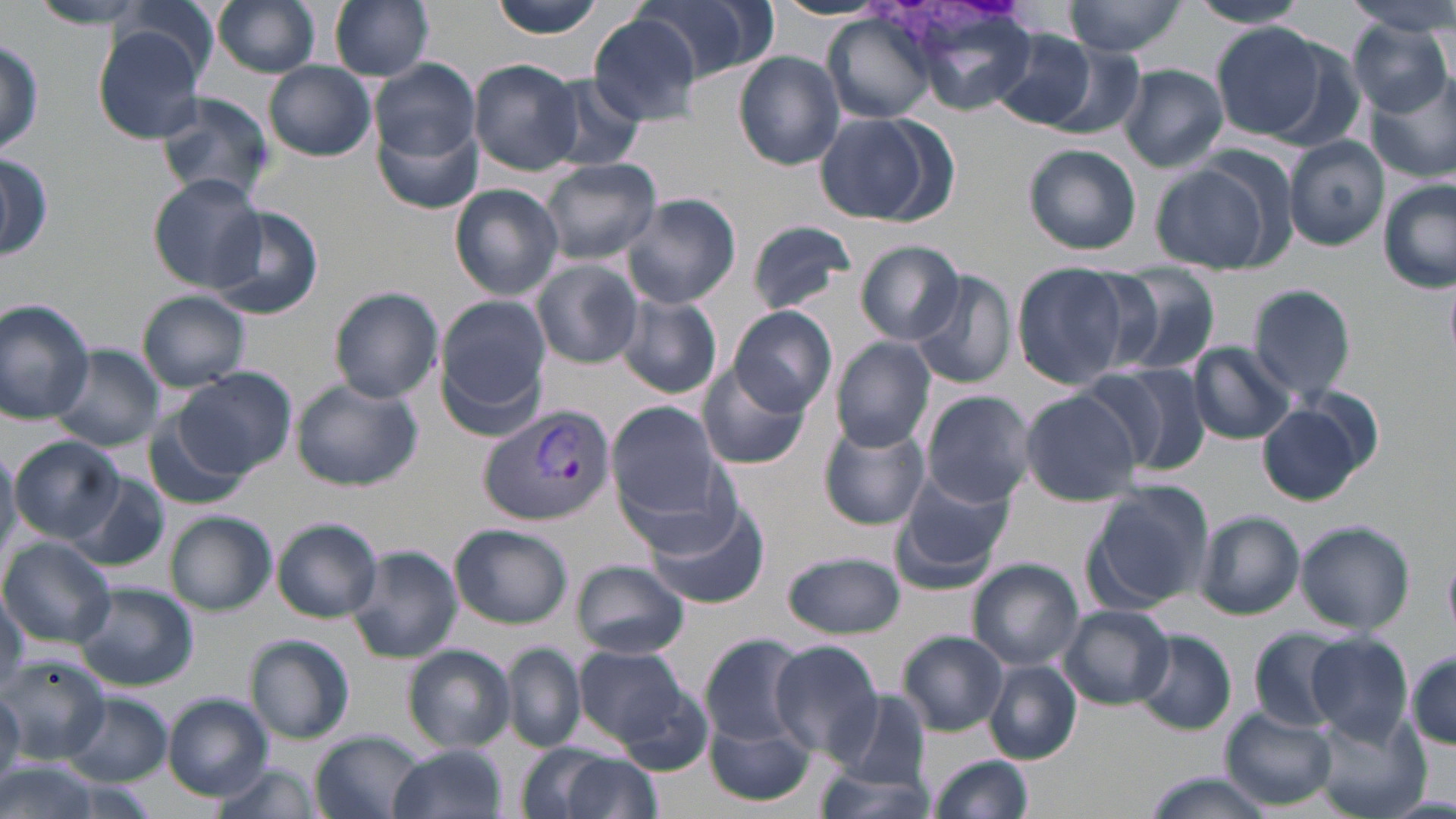
Approximate bounding boxes as (x1, y1, x2, y2) in pixels. Uninfected red blood cell locations: (28, 0, 160, 30), (211, 0, 325, 77), (330, 0, 435, 81), (487, 0, 610, 39), (634, 0, 771, 85), (1064, 0, 1189, 58), (1346, 0, 1456, 37), (1189, 1, 1311, 30), (116, 2, 219, 87), (223, 2, 346, 158), (771, 2, 889, 21), (902, 5, 1042, 117), (588, 14, 702, 124), (827, 15, 939, 123), (1348, 18, 1454, 115), (1211, 24, 1326, 139), (93, 28, 206, 142), (987, 28, 1100, 131), (1, 35, 44, 156), (734, 51, 845, 169), (372, 58, 480, 163), (264, 61, 376, 161), (471, 61, 584, 175), (1119, 64, 1229, 171), (1368, 74, 1456, 184), (539, 75, 648, 171), (153, 90, 278, 206), (376, 112, 484, 217), (814, 112, 938, 224), (1284, 137, 1388, 250), (1024, 144, 1141, 255), (0, 151, 52, 263), (542, 158, 661, 263), (1152, 159, 1277, 272), (148, 174, 265, 292), (1377, 181, 1454, 293), (449, 185, 564, 299), (620, 192, 742, 310), (208, 208, 324, 322), (744, 219, 856, 314), (855, 241, 965, 345), (533, 259, 644, 368), (1011, 264, 1130, 389), (1098, 265, 1224, 380), (909, 271, 1018, 389), (1248, 284, 1356, 398), (330, 287, 445, 403), (137, 292, 251, 390), (616, 293, 723, 399), (436, 296, 550, 425), (0, 299, 98, 425), (731, 306, 838, 417), (831, 339, 937, 450), (1188, 342, 1295, 443), (47, 344, 165, 453), (698, 363, 812, 471), (1085, 363, 1210, 476), (175, 366, 294, 478), (292, 378, 422, 491), (1019, 390, 1141, 506), (921, 391, 1035, 508), (607, 401, 735, 531), (1258, 401, 1369, 505), (146, 417, 244, 510), (816, 420, 930, 530), (10, 436, 121, 542), (0, 439, 22, 566), (894, 469, 1016, 583), (71, 475, 171, 571), (1084, 481, 1214, 610), (646, 502, 770, 611), (1195, 511, 1303, 620), (166, 512, 276, 614), (273, 518, 382, 622), (1295, 521, 1416, 634), (450, 523, 572, 629), (2, 538, 116, 646), (345, 542, 463, 664), (1444, 548, 1456, 637), (780, 551, 907, 639), (968, 559, 1083, 672), (572, 560, 691, 660), (77, 583, 198, 691), (0, 591, 28, 701), (1059, 605, 1174, 708), (1249, 628, 1350, 731), (898, 630, 1010, 736), (1132, 630, 1237, 735), (699, 633, 809, 745), (1305, 633, 1413, 742), (246, 634, 357, 745), (768, 641, 883, 757), (503, 645, 587, 752), (574, 645, 696, 744), (404, 647, 515, 751), (1406, 650, 1456, 749), (0, 654, 110, 761), (986, 661, 1082, 764), (608, 678, 718, 776), (829, 690, 931, 790), (0, 691, 24, 789), (66, 692, 171, 786), (161, 693, 274, 801), (1221, 708, 1338, 811), (704, 713, 817, 808), (1314, 713, 1426, 819), (310, 730, 424, 819), (387, 744, 512, 819), (524, 746, 658, 819), (925, 753, 1035, 819), (0, 755, 101, 819), (210, 761, 321, 819), (812, 763, 938, 818), (1143, 772, 1279, 819). Plasmodium vivax-infected red blood cell locations: (478, 405, 617, 527). Slide-level diagnosis: Plasmodium vivax. Light microscopy. Image is 1456×819 pixels. One field of a larger specimen. May-Grünwald-Giemsa-stained preparation. Thin blood film. 1000x magnification.